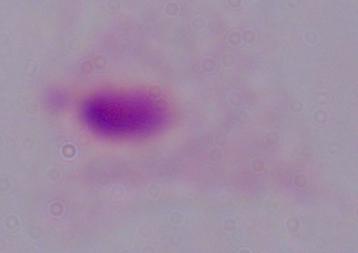
Micrograph. Captured at 1000x magnification. A trichomonad is seen.